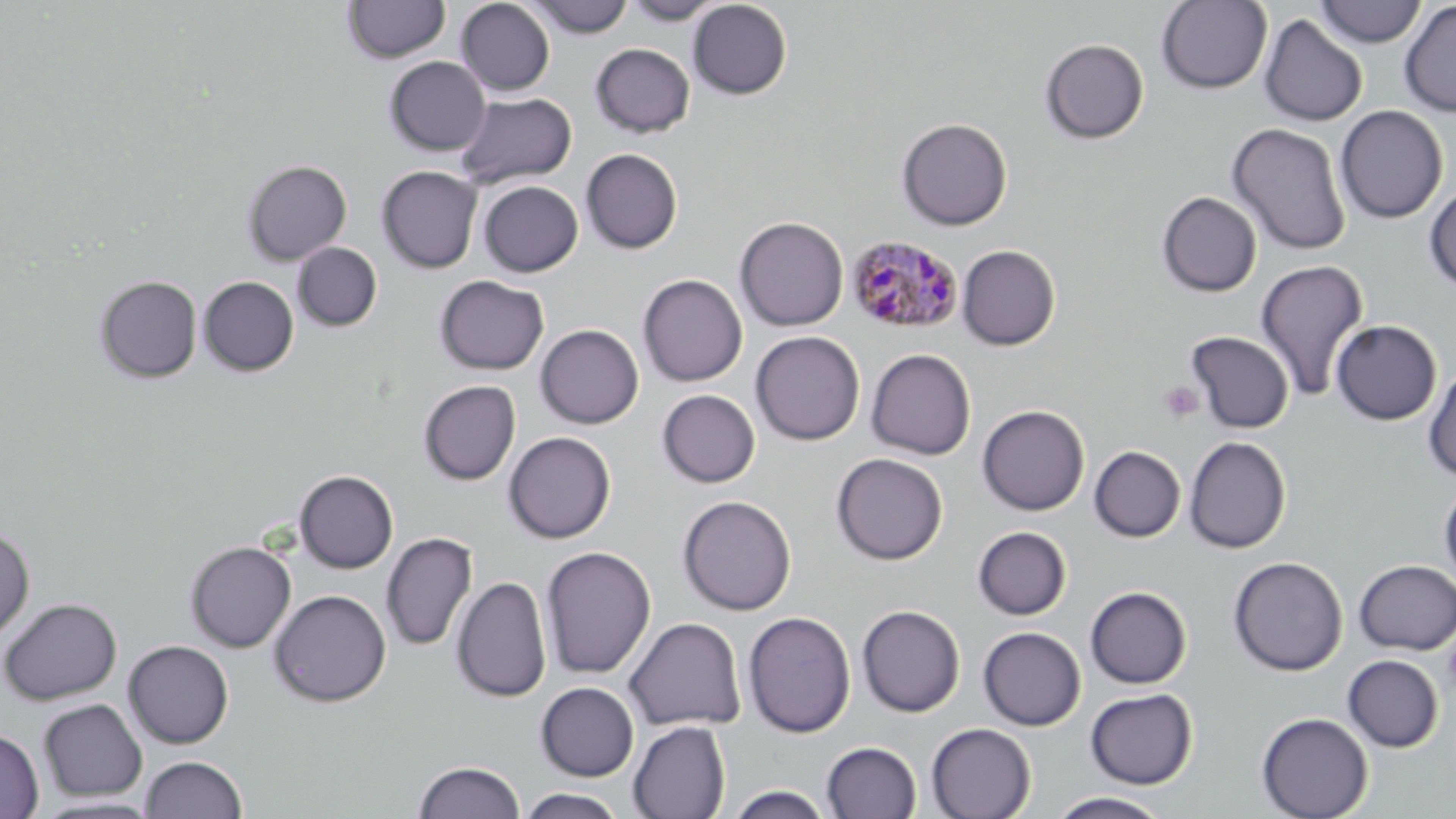 Approximate bounding boxes as [x1, y1, x2, y2] in pixels. Uninfected red blood cell locations: [343, 0, 450, 63], [455, 0, 555, 96], [525, 0, 634, 38], [622, 0, 725, 25], [688, 0, 792, 99], [1156, 1, 1272, 94], [1316, 1, 1426, 47], [1399, 1, 1456, 117], [1260, 14, 1368, 126], [1039, 38, 1149, 144], [590, 43, 695, 138], [384, 56, 490, 156], [455, 92, 577, 189], [1335, 105, 1448, 224], [896, 117, 1012, 230], [1226, 123, 1351, 256], [580, 148, 683, 254], [242, 159, 352, 266], [377, 166, 483, 273], [478, 181, 583, 277], [1423, 183, 1456, 293], [1157, 192, 1262, 297], [734, 216, 849, 332], [292, 242, 382, 332], [957, 245, 1060, 350], [1254, 260, 1369, 401], [638, 274, 748, 387], [94, 275, 202, 383], [434, 275, 549, 375], [198, 276, 299, 376], [1331, 319, 1442, 425], [535, 324, 644, 429], [750, 331, 865, 445], [1186, 331, 1294, 434], [866, 348, 976, 460], [1422, 362, 1456, 483], [418, 380, 521, 485], [657, 389, 761, 488], [977, 405, 1090, 516], [503, 431, 616, 543], [1184, 436, 1291, 553], [1089, 446, 1186, 542], [831, 453, 947, 565], [294, 470, 398, 573], [1438, 479, 1456, 591], [678, 495, 796, 615], [0, 523, 35, 644], [972, 526, 1071, 620], [381, 532, 477, 651], [185, 541, 296, 652], [540, 545, 657, 680], [1228, 556, 1348, 676], [1353, 560, 1456, 654], [451, 575, 551, 703], [1085, 586, 1192, 689], [269, 589, 391, 707], [0, 597, 122, 705], [857, 605, 965, 717], [742, 610, 856, 738], [624, 616, 747, 731], [978, 626, 1086, 730], [124, 640, 234, 748], [1342, 655, 1444, 753], [535, 682, 640, 782], [1085, 688, 1197, 789], [38, 698, 147, 801], [1256, 712, 1374, 819], [628, 720, 730, 819], [926, 723, 1036, 819], [0, 729, 43, 818], [821, 741, 922, 819], [140, 755, 248, 818], [413, 760, 526, 818], [723, 786, 836, 819], [515, 789, 629, 819], [1046, 792, 1173, 819], [31, 796, 166, 817]. Platelet locations: [1158, 381, 1204, 423], [1442, 634, 1456, 696]. Plasmodium malariae-infected red blood cell locations: [845, 234, 964, 334]. Slide-level diagnosis: Plasmodium malariae. Optical microscopy. One field of a larger specimen. Image is 1456×819 pixels. Captured at 1000x magnification. May-Grünwald-Giemsa stain. Thin blood smear.